Report the malaria status of this cell.
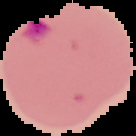

It is parasitized.

Summary:
  - Preparation: thin blood smear
  - Image type: segmented cell region on a black background
  - Image size: 136×136 pixels